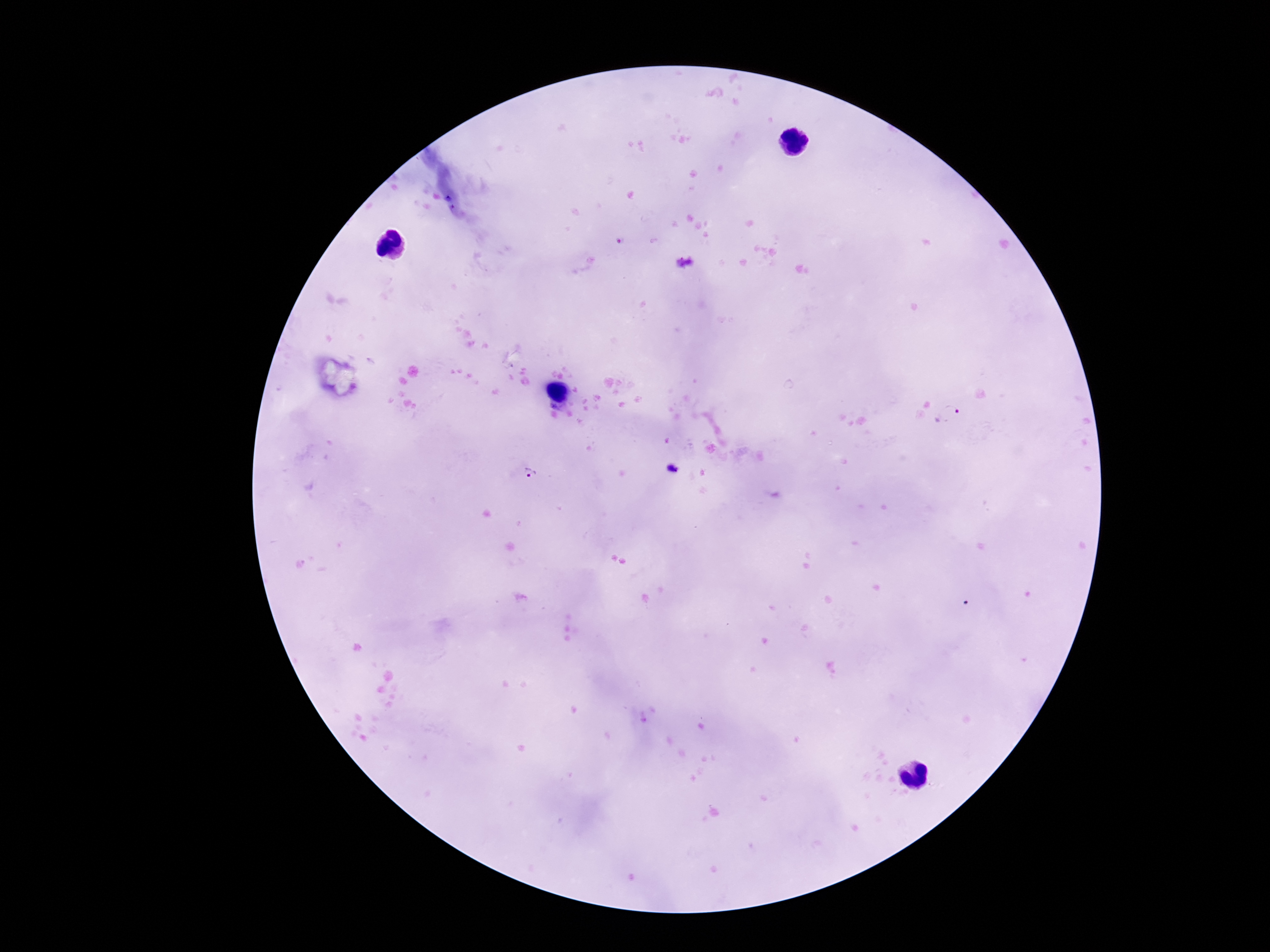

magnification = 100x
stain = Giemsa
capture = smartphone camera through the microscope eyepiece
Plasmodium parasite locations = approximate centers as (x, y) in pixels: (948, 415), (672, 470), (530, 473)
image size = 1270×952 pixels
field of view = one from this slide
patient malaria status = infected
preparation = thick blood film